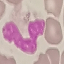

result = no malaria parasites seen
capture = smartphone camera at the microscope eyepiece
stain = Giemsa
preparation = thin smear
image type = cell patch, automatically extracted from a larger field of view and resized to 64 × 64 pixels